Outline each Trypanosoma brucei.
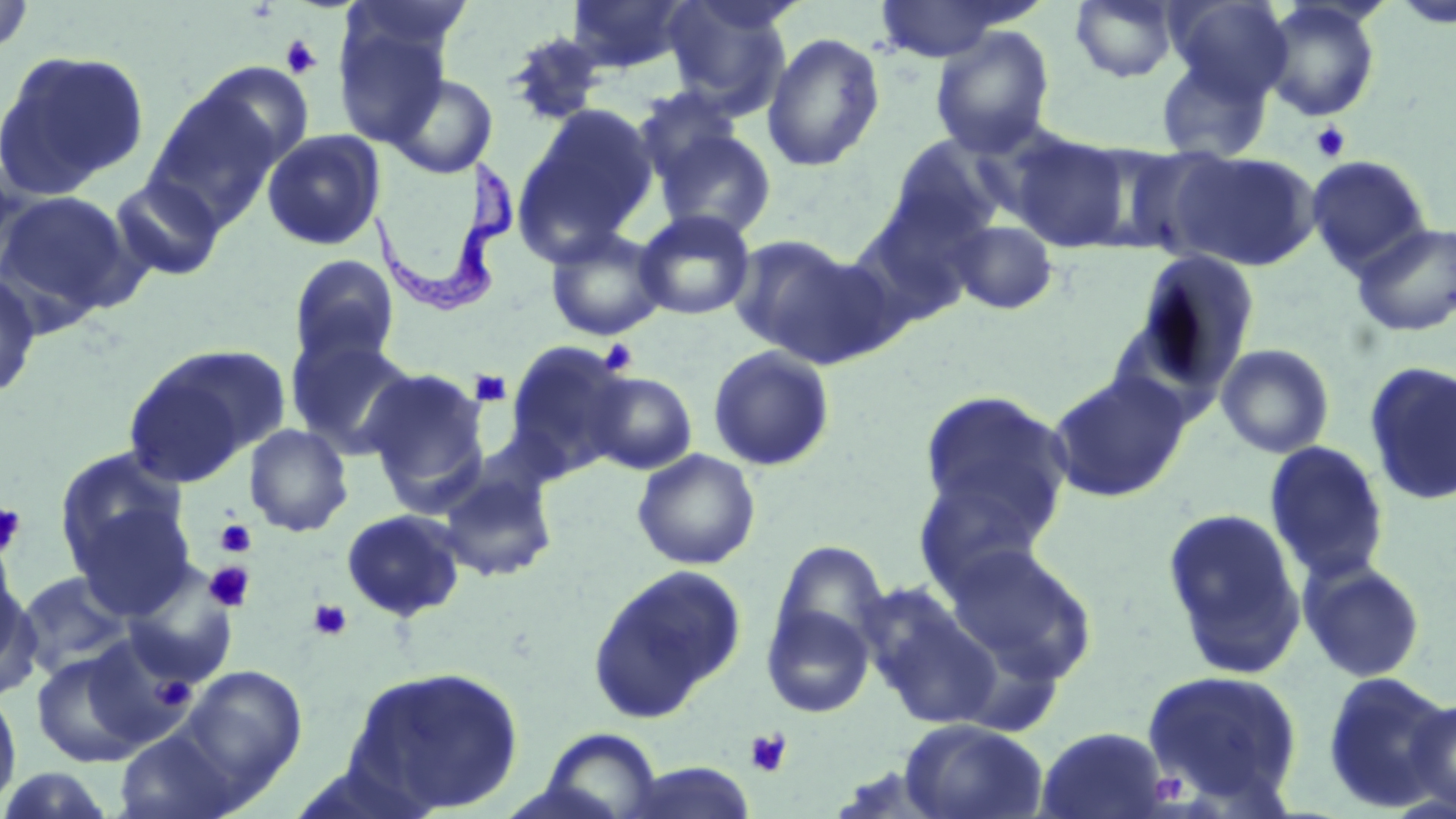
Approximate bounding boxes as (x1, y1, x2, y2) in pixels.
Trypanosoma brucei: (365, 161, 519, 318).

Uninfected red blood cell locations: (1, 0, 35, 57), (566, 0, 694, 73), (663, 0, 795, 113), (1071, 0, 1179, 83), (1168, 0, 1293, 102), (1390, 0, 1456, 30), (875, 1, 1013, 62), (1261, 2, 1382, 122), (333, 16, 453, 148), (929, 25, 1055, 158), (504, 31, 607, 127), (762, 31, 885, 172), (0, 49, 150, 197), (1155, 55, 1272, 162), (191, 63, 316, 174), (386, 73, 496, 178), (147, 86, 284, 224), (633, 86, 745, 186), (516, 103, 660, 257), (654, 128, 776, 240), (261, 129, 386, 251), (1009, 134, 1130, 252), (886, 136, 1006, 245), (1098, 144, 1242, 260), (1168, 150, 1321, 272), (1305, 155, 1431, 274), (0, 161, 34, 280), (109, 176, 226, 282), (0, 191, 138, 320), (851, 200, 983, 329), (635, 209, 756, 321), (947, 219, 1058, 315), (1350, 221, 1456, 337), (545, 227, 668, 342), (727, 235, 857, 357), (769, 247, 906, 368), (1131, 250, 1262, 391), (288, 254, 401, 368), (0, 272, 42, 401), (286, 333, 418, 457), (505, 340, 634, 478), (1215, 343, 1335, 459), (708, 345, 835, 472), (124, 346, 284, 482), (1363, 361, 1456, 507), (364, 367, 490, 506), (1047, 370, 1192, 503), (585, 371, 697, 475), (918, 389, 1074, 546), (244, 424, 353, 537), (1263, 440, 1390, 584), (53, 446, 189, 576), (632, 449, 761, 570), (435, 464, 558, 582), (911, 473, 1057, 599), (68, 500, 199, 619), (1161, 507, 1307, 679), (340, 509, 467, 622), (769, 541, 891, 669), (943, 543, 1098, 681), (0, 553, 35, 697), (1299, 559, 1428, 684), (588, 563, 748, 721), (16, 571, 135, 678), (123, 576, 235, 688), (868, 598, 1003, 730), (762, 602, 876, 718), (83, 633, 197, 749), (31, 649, 151, 768), (342, 664, 524, 816), (178, 665, 307, 795), (1142, 668, 1304, 809), (1321, 671, 1452, 811), (0, 684, 22, 814), (1403, 697, 1456, 815), (899, 719, 1049, 819), (1035, 726, 1171, 819), (115, 729, 239, 818), (538, 729, 665, 819), (615, 763, 758, 819), (0, 767, 118, 817). Platelet locations: (280, 34, 322, 79), (1310, 121, 1350, 162), (599, 339, 639, 375), (469, 369, 512, 406), (0, 502, 26, 557), (215, 519, 256, 558), (203, 561, 255, 612), (308, 599, 351, 641), (153, 675, 197, 710), (744, 729, 792, 777). Slide-level diagnosis: Trypanosoma brucei. Light microscopy. Captured at 1000x magnification. May-Grünwald-Giemsa-stained preparation. Thin blood film. Single field of view. Image is 1456×819 pixels.